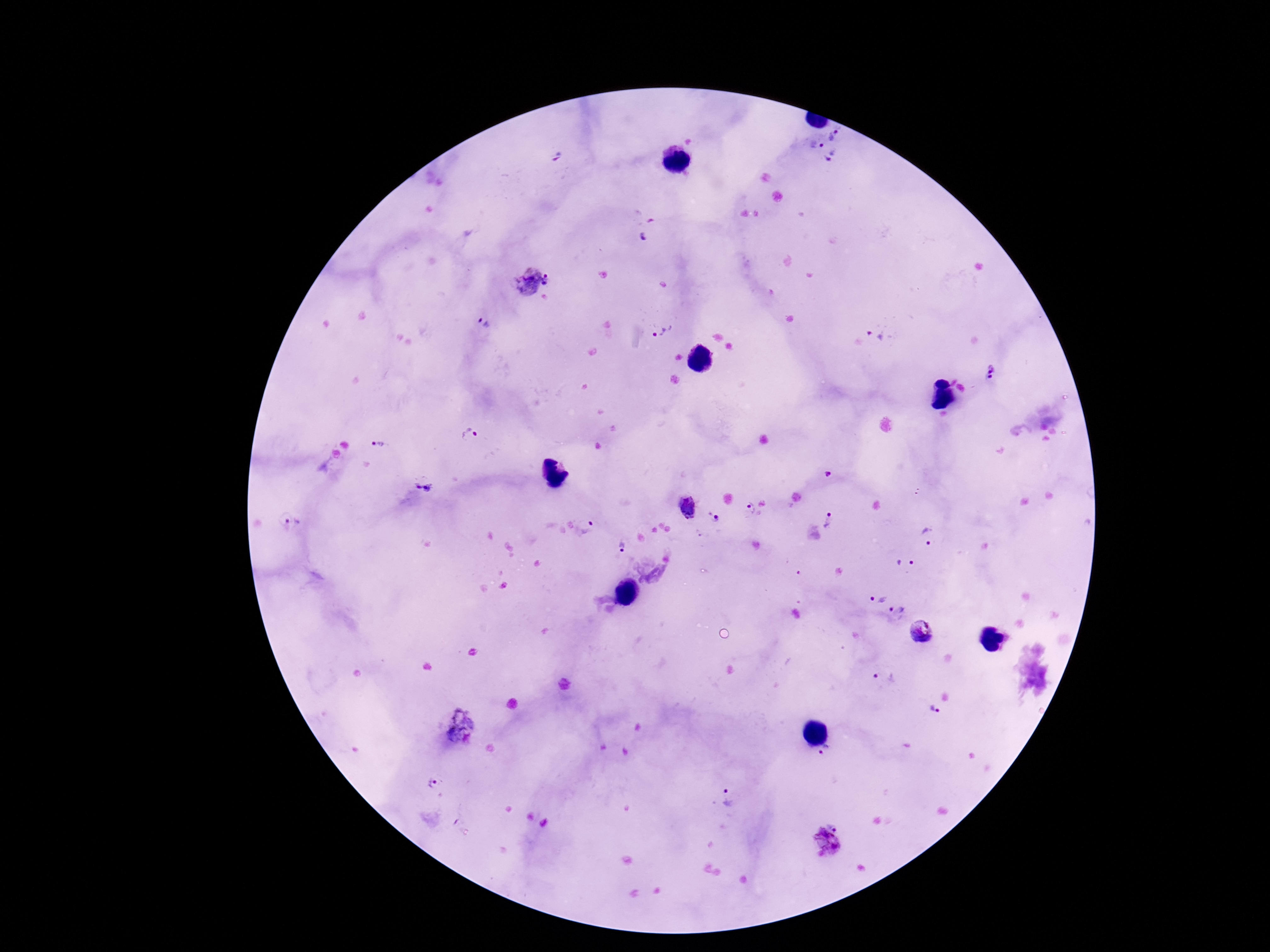

magnification: 100x
field_of_view: one from this slide
patient_malaria_status: positive
preparation: thick blood film
stain: Giemsa
plasmodium_parasite_locations: 'approximate object centers, in pixels from the top-left corner: (x=834, y=135), (x=815, y=145), (x=832, y=159), (x=644, y=238), (x=550, y=280), (x=526, y=281), (x=483, y=323), (x=664, y=332), (x=873, y=336), (x=991, y=368), (x=991, y=377), (x=470, y=434), (x=376, y=446), (x=828, y=474), (x=425, y=490), (x=917, y=491), (x=687, y=506), (x=750, y=507), (x=716, y=518), (x=830, y=521), (x=291, y=523), (x=587, y=527), (x=928, y=537), (x=624, y=547), (x=904, y=564), (x=876, y=598), (x=897, y=611), (x=922, y=631), (x=886, y=678), (x=934, y=709), (x=455, y=711), (x=464, y=736), (x=826, y=751), (x=435, y=785), (x=727, y=798), (x=836, y=828), (x=825, y=844)'
capture: smartphone camera through the microscope eyepiece
image_size: 1270×952 pixels